Give the position of every leukocyte visible.
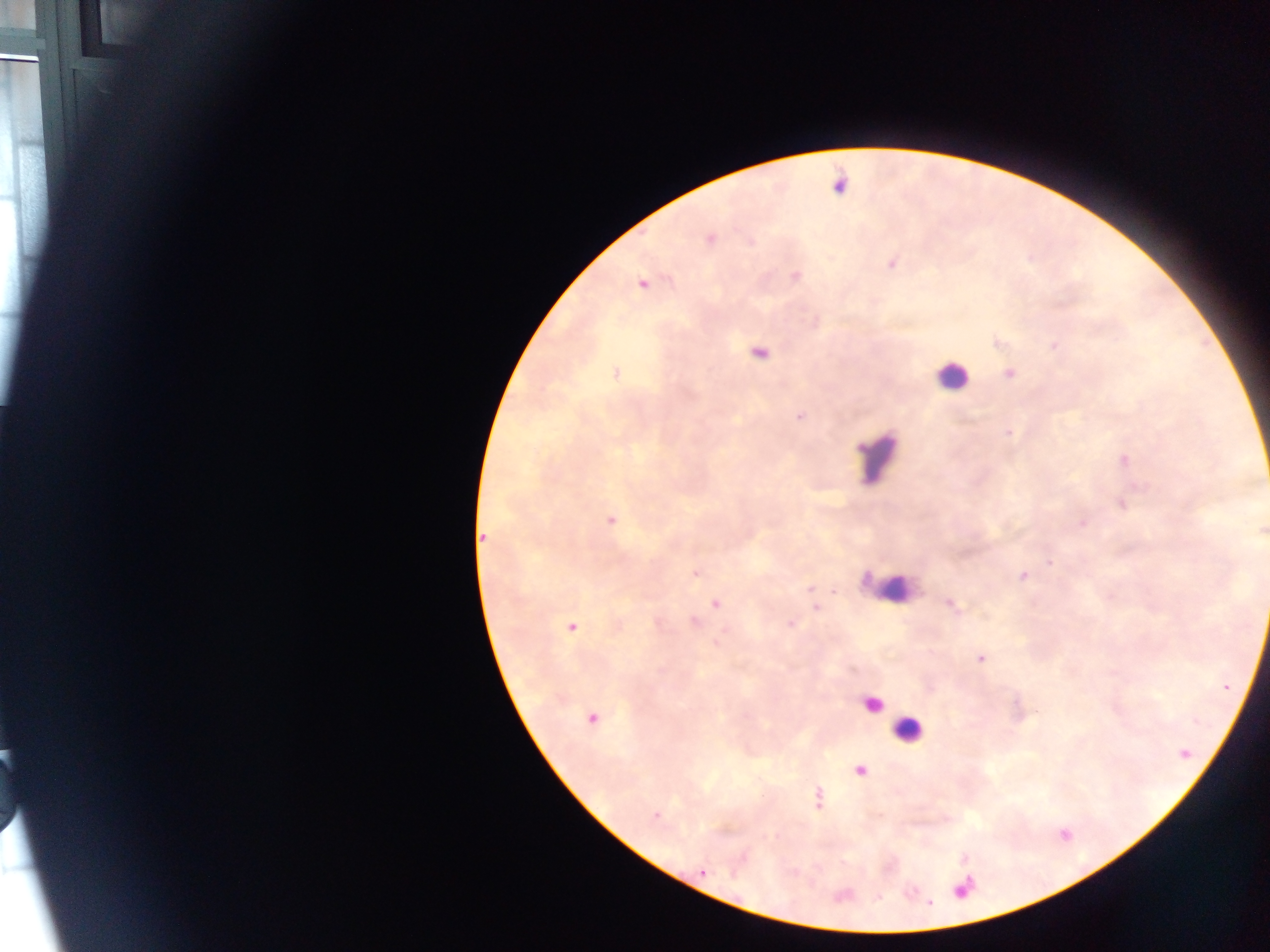
Approximate centers as {x, y} in pixels.
Leukocytes: {947, 380}, {894, 589}, {878, 710}, {910, 735}.

Plasmodium parasite locations: {615, 373}, {799, 417}, {1006, 432}, {610, 519}, {483, 535}, {1049, 561}, {695, 573}, {1022, 575}, {808, 589}, {832, 590}, {948, 602}, {715, 605}, {814, 607}, {572, 626}, {979, 657}, {591, 719}, {860, 769}, {818, 798}, {703, 870}. Thick blood smear. Image is 1270×952 pixels. Sample from Ghana. One field of view. Photographed through a microscope with a mobile-phone camera.